Assess this cell for malaria.
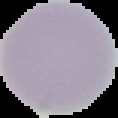
Uninfected.

From a thin blood film. Image is 118×118 pixels. Segmented cell region on a black background.